Identify the parasite.
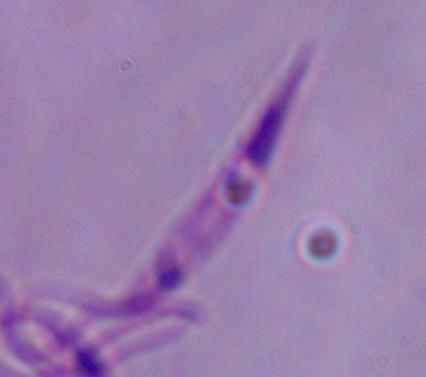

This is Leishmania.

modality = photomicrograph
magnification = 1000x